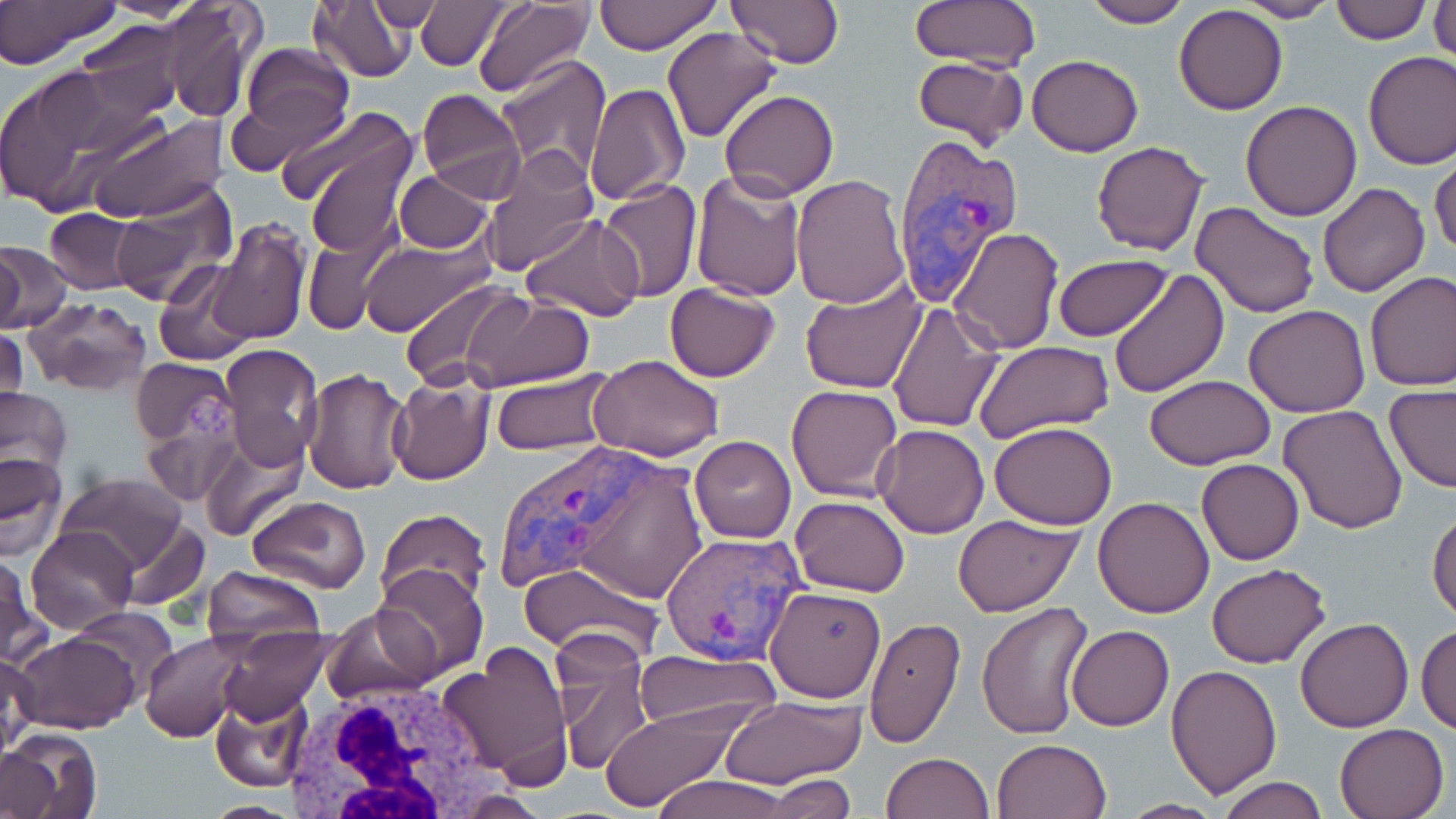

Summary:
  - Coordinate format: approximate bounding boxes as [x1, y1, x2, y2] in pixels
  - Plasmodium vivax-infected red blood cell locations: [889, 138, 1023, 298], [493, 439, 706, 603], [660, 531, 809, 666]
  - Uninfected red blood cell locations: [0, 0, 124, 71], [154, 0, 264, 125], [307, 0, 417, 85], [363, 0, 445, 36], [593, 0, 722, 53], [724, 0, 845, 68], [907, 0, 1042, 71], [1236, 0, 1341, 22], [413, 1, 518, 73], [1079, 1, 1193, 28], [1331, 1, 1433, 45], [1428, 1, 1456, 60], [471, 2, 596, 96], [1174, 4, 1289, 115], [77, 23, 186, 124], [661, 27, 782, 145], [233, 43, 356, 161], [1362, 49, 1456, 169], [911, 54, 1028, 152], [1028, 55, 1144, 156], [496, 57, 613, 182], [0, 63, 164, 217], [585, 82, 691, 208], [418, 88, 525, 202], [720, 89, 837, 200], [1242, 101, 1362, 221], [85, 112, 227, 224], [294, 113, 420, 256], [1091, 141, 1211, 256], [478, 148, 600, 275], [1430, 153, 1456, 261], [394, 171, 493, 254], [690, 171, 809, 301], [789, 174, 910, 309], [596, 181, 703, 301], [1316, 182, 1431, 298], [111, 186, 235, 308], [1191, 200, 1321, 319], [44, 208, 141, 295], [519, 214, 644, 322], [208, 217, 311, 346], [949, 228, 1064, 355], [302, 232, 389, 337], [360, 239, 493, 336], [0, 241, 71, 333], [1052, 254, 1176, 342], [152, 260, 258, 367], [1107, 269, 1228, 398], [1364, 270, 1456, 391], [399, 278, 527, 390], [799, 279, 928, 395], [663, 282, 780, 382], [463, 294, 592, 391], [25, 297, 151, 395], [886, 300, 1004, 433], [1243, 304, 1370, 417], [0, 322, 27, 419], [974, 340, 1114, 440], [218, 344, 323, 469], [589, 354, 724, 459], [132, 358, 237, 448], [301, 367, 413, 495], [490, 370, 618, 454], [388, 373, 495, 484], [1145, 375, 1276, 468], [786, 383, 904, 501], [1384, 385, 1456, 494], [0, 387, 72, 478], [1277, 405, 1408, 534], [142, 413, 239, 508], [989, 422, 1117, 529], [873, 424, 990, 538], [200, 433, 307, 541], [689, 435, 797, 543], [0, 454, 68, 558], [1197, 459, 1304, 566], [55, 472, 190, 579], [243, 494, 371, 595], [792, 495, 909, 598], [1093, 497, 1215, 619], [1427, 505, 1456, 622], [377, 510, 491, 608], [953, 513, 1086, 618], [120, 519, 209, 612], [25, 525, 139, 633], [0, 555, 49, 672], [519, 561, 666, 660], [372, 563, 489, 683], [1206, 564, 1331, 668], [200, 565, 326, 651], [765, 586, 885, 701], [975, 601, 1096, 743], [323, 603, 439, 705], [70, 606, 181, 700], [865, 616, 967, 749], [1295, 616, 1414, 733], [1416, 623, 1456, 733], [217, 624, 333, 727], [1066, 626, 1175, 731], [11, 630, 140, 734], [551, 630, 654, 775], [140, 632, 251, 742], [442, 640, 573, 786], [636, 649, 782, 731], [1, 653, 38, 757], [1167, 663, 1283, 798], [210, 694, 312, 794], [719, 698, 864, 790], [598, 709, 739, 813], [1334, 722, 1450, 818], [4, 730, 102, 818], [990, 738, 1113, 819], [0, 751, 57, 819], [881, 751, 994, 819], [767, 774, 856, 817], [646, 775, 800, 819], [1216, 777, 1327, 819], [202, 799, 302, 817], [1115, 799, 1226, 817]
  - White blood cell locations: [277, 675, 503, 819]
  - Slide-level diagnosis: Plasmodium vivax
  - Stain: May-Grünwald-Giemsa
  - Field of view: single
  - Image size: 1456×819 pixels
  - Preparation: thin blood smear
  - Modality: light microscopy
  - Magnification: 1000x